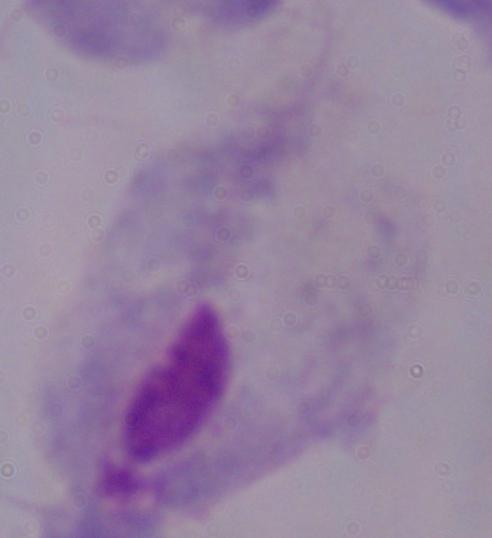

identification: trichomonad
modality: photomicrograph
magnification: 1000x